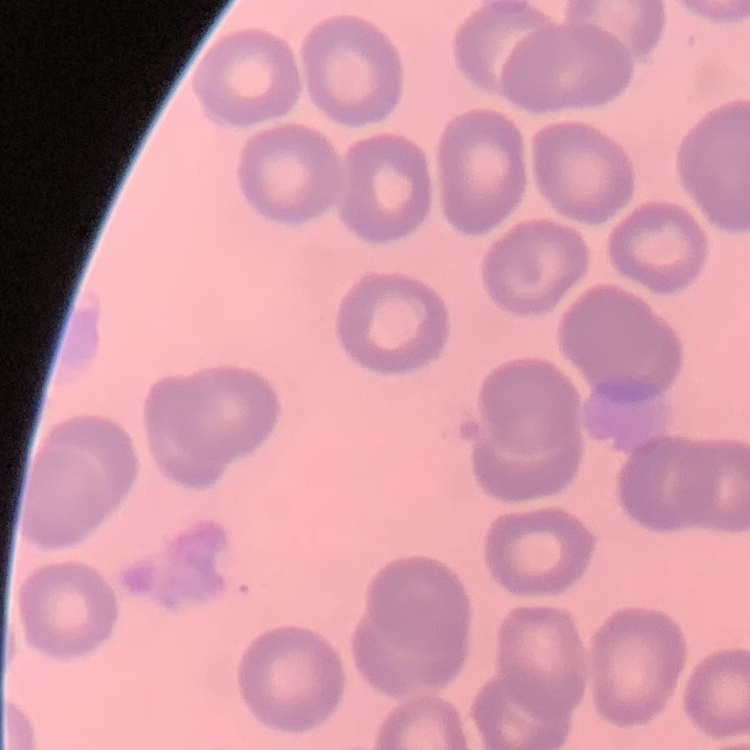 The red blood cells exhibit no rouleaux formation. Stained with either Field's or Giemsa. Thin peripheral smear. One tile cut from a larger photomicrograph.